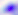
Summary:
  - Modality: photomicrograph
  - Magnification: 400x
  - Identification: Toxoplasma gondii